Assess the morphology of the red blood cells.
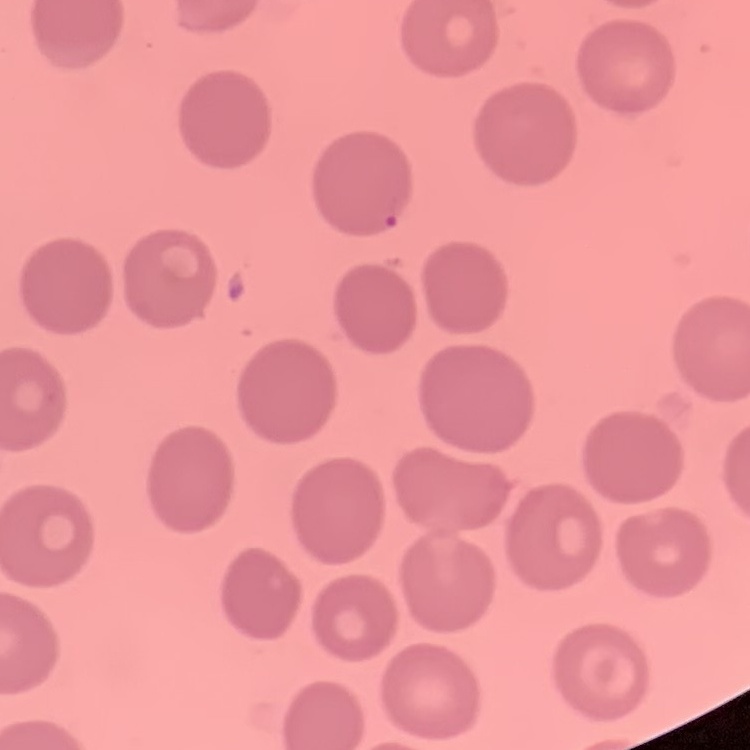
No rouleaux formation.

Summary:
  - Stain: Field's or Giemsa
  - Image type: square crop of a larger photomicrograph
  - Preparation: thin blood film